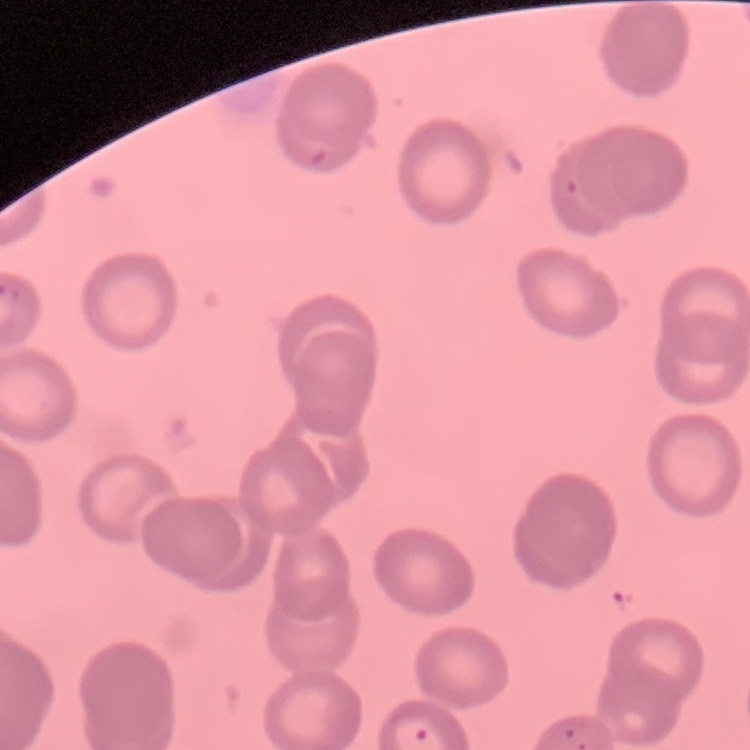

{
  "red_blood_cell_morphology": "no rouleaux formation",
  "stain": "Field's or Giemsa",
  "image_type": "square crop of a larger photomicrograph",
  "preparation": "thin peripheral smear"
}